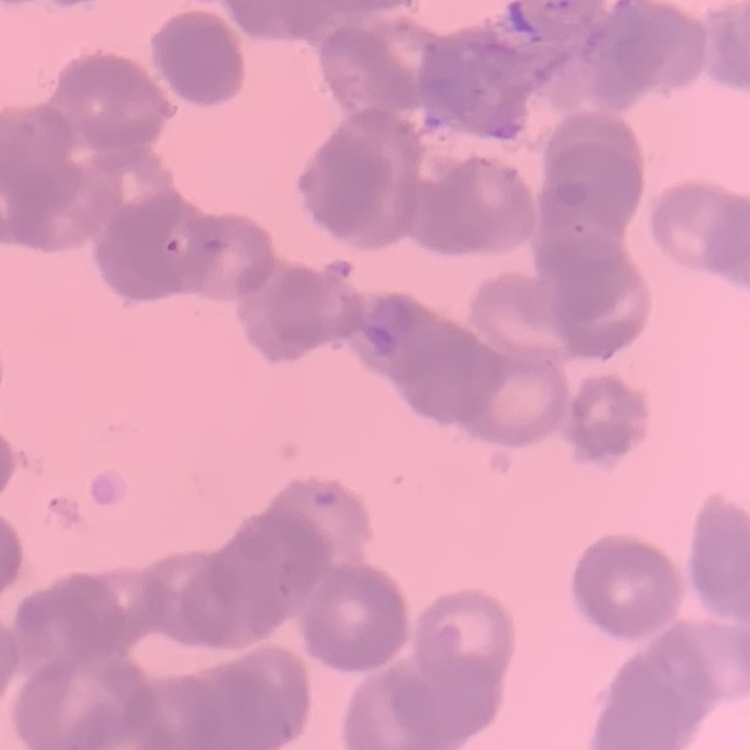
{
  "red_blood_cell_morphology": "rouleaux formation",
  "stain": "Field's or Giemsa",
  "image_type": "square crop of a larger photomicrograph",
  "preparation": "thin blood smear"
}